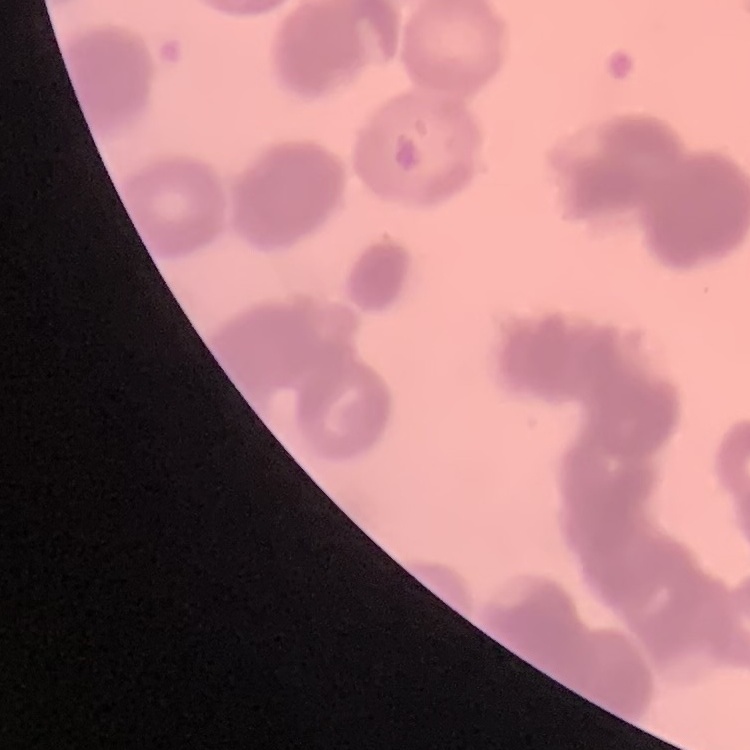
erythrocyte morphology = rouleaux formation
preparation = thin blood film
image type = square crop of a larger photomicrograph
stain = Field's or Giemsa